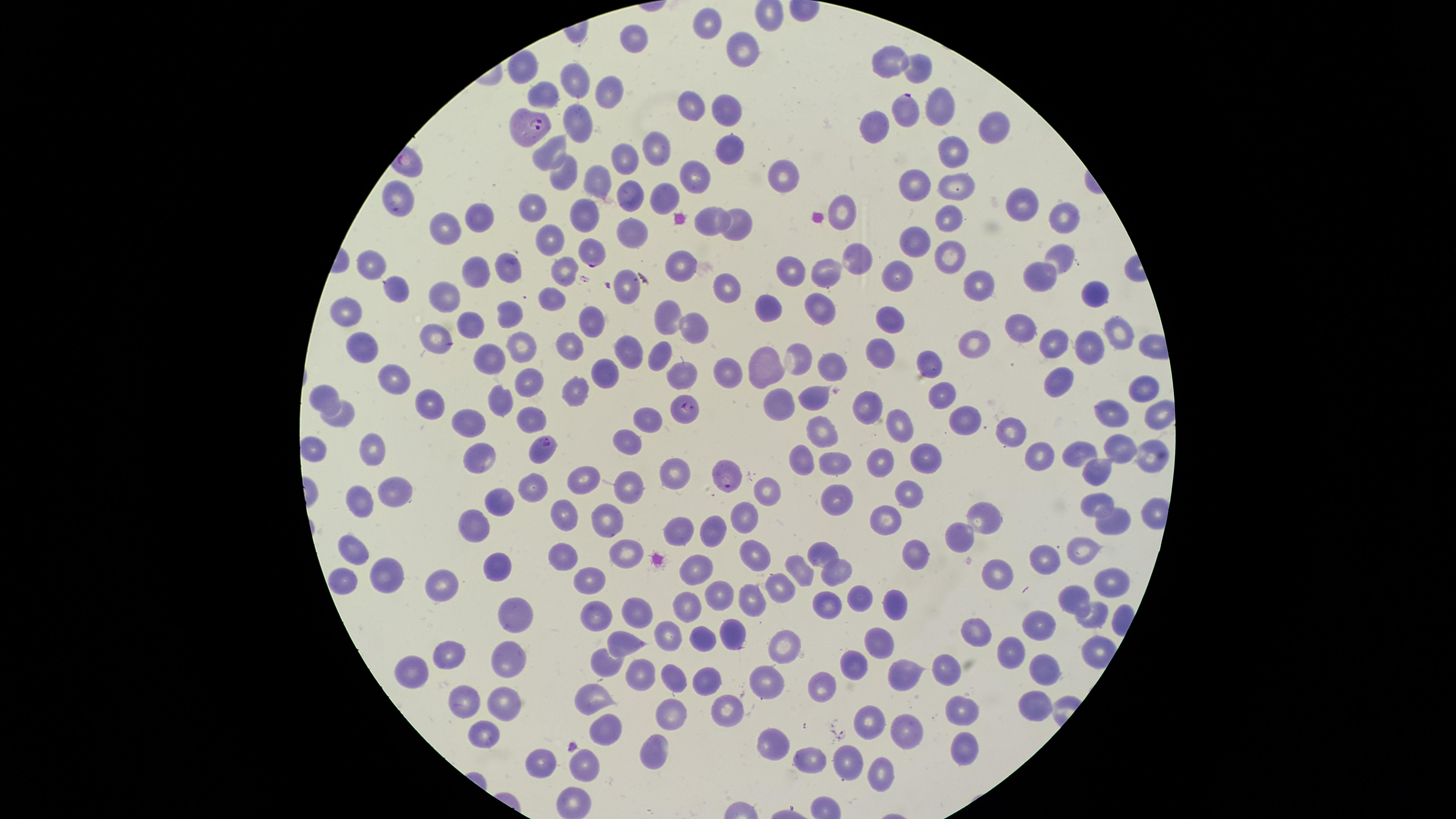
uninfected red blood cells = approximate marker points as {x, y} in pixels: {707, 24}, {632, 42}, {744, 47}, {890, 59}, {921, 61}, {528, 70}, {575, 82}, {609, 90}, {543, 94}, {691, 98}, {935, 105}, {731, 112}, {578, 119}, {875, 122}, {995, 127}, {552, 147}, {955, 148}, {652, 149}, {728, 155}, {623, 161}, {561, 173}, {694, 175}, {593, 178}, {782, 179}, {922, 181}, {950, 182}, {625, 193}, {396, 199}, {655, 200}, {534, 205}, {1020, 207}, {847, 211}, {737, 215}, {951, 215}, {582, 216}, {482, 217}, {1059, 221}, {705, 223}, {442, 227}, {630, 233}, {556, 238}, {911, 240}, {1062, 255}, {851, 256}, {953, 257}, {373, 264}, {685, 267}, {504, 270}, {476, 272}, {788, 273}, {896, 273}, {566, 275}, {1040, 276}, {820, 278}, {979, 279}, {624, 289}, {397, 290}, {727, 290}, {552, 296}, {448, 298}, {1093, 299}, {817, 302}, {353, 303}, {766, 307}, {504, 309}, {887, 315}, {672, 319}, {592, 323}, {467, 324}, {694, 325}, {1025, 330}, {1119, 332}, {429, 338}, {523, 339}, {1053, 342}, {970, 345}, {878, 346}, {370, 349}, {1088, 349}, {626, 351}, {802, 351}, {571, 352}, {663, 353}, {493, 358}, {770, 364}, {929, 364}, {827, 366}, {727, 370}, {604, 374}, {397, 375}, {677, 375}, {529, 380}, {1058, 381}, {1138, 388}, {575, 389}, {809, 391}, {942, 392}, {321, 395}, {499, 398}, {433, 402}, {777, 402}, {868, 402}, {349, 413}, {1109, 413}, {531, 416}, {963, 416}, {471, 419}, {645, 423}, {819, 427}, {902, 427}, {1009, 428}, {373, 447}, {630, 447}, {1115, 447}, {1037, 448}, {1083, 451}, {482, 453}, {925, 453}, {1148, 453}, {315, 456}, {802, 458}, {835, 462}, {877, 462}, {672, 471}, {587, 477}, {528, 483}, {627, 483}, {394, 490}, {768, 490}, {832, 501}, {912, 501}, {1096, 501}, {362, 504}, {495, 504}, {988, 514}, {745, 515}, {561, 516}, {612, 516}, {881, 524}, {1113, 524}, {475, 525}, {716, 526}, {681, 530}, {970, 535}, {822, 545}, {356, 549}, {625, 549}, {915, 551}, {748, 552}, {1079, 555}, {564, 558}, {695, 560}, {1051, 561}, {499, 563}, {800, 568}, {394, 572}, {1007, 573}, {835, 574}, {343, 577}, {592, 581}, {1106, 581}, {444, 584}, {781, 588}, {719, 594}, {1075, 595}, {752, 596}, {823, 601}, {858, 601}, {894, 604}, {689, 608}, {517, 609}, {1094, 612}, {637, 613}, {599, 617}, {1039, 626}, {981, 630}, {670, 633}, {735, 634}, {700, 636}, {881, 643}, {621, 644}, {789, 647}, {1015, 651}, {450, 653}, {509, 657}, {858, 657}, {604, 663}, {1044, 664}, {945, 667}, {644, 668}, {906, 670}, {714, 672}, {673, 674}, {404, 678}, {765, 679}, {826, 683}, {589, 697}, {503, 702}, {1030, 705}, {464, 706}, {725, 709}, {674, 711}, {969, 712}, {873, 720}, {606, 729}, {482, 735}, {901, 737}, {776, 740}, {654, 743}, {956, 744}, {812, 759}, {849, 759}, {580, 764}, {542, 765}, {876, 768}, {569, 799}
preparation = thin blood smear
field of view = single
presence = malaria parasites identified
capture = smartphone photograph through the microscope eyepiece
stain = Giemsa
parasitized red blood cells = approximate marker points as {x, y} in pixels: {909, 113}, {529, 132}, {590, 253}, {687, 409}, {544, 449}, {727, 476}
species = Plasmodium falciparum
visible region = circular
image size = 1456×819 pixels